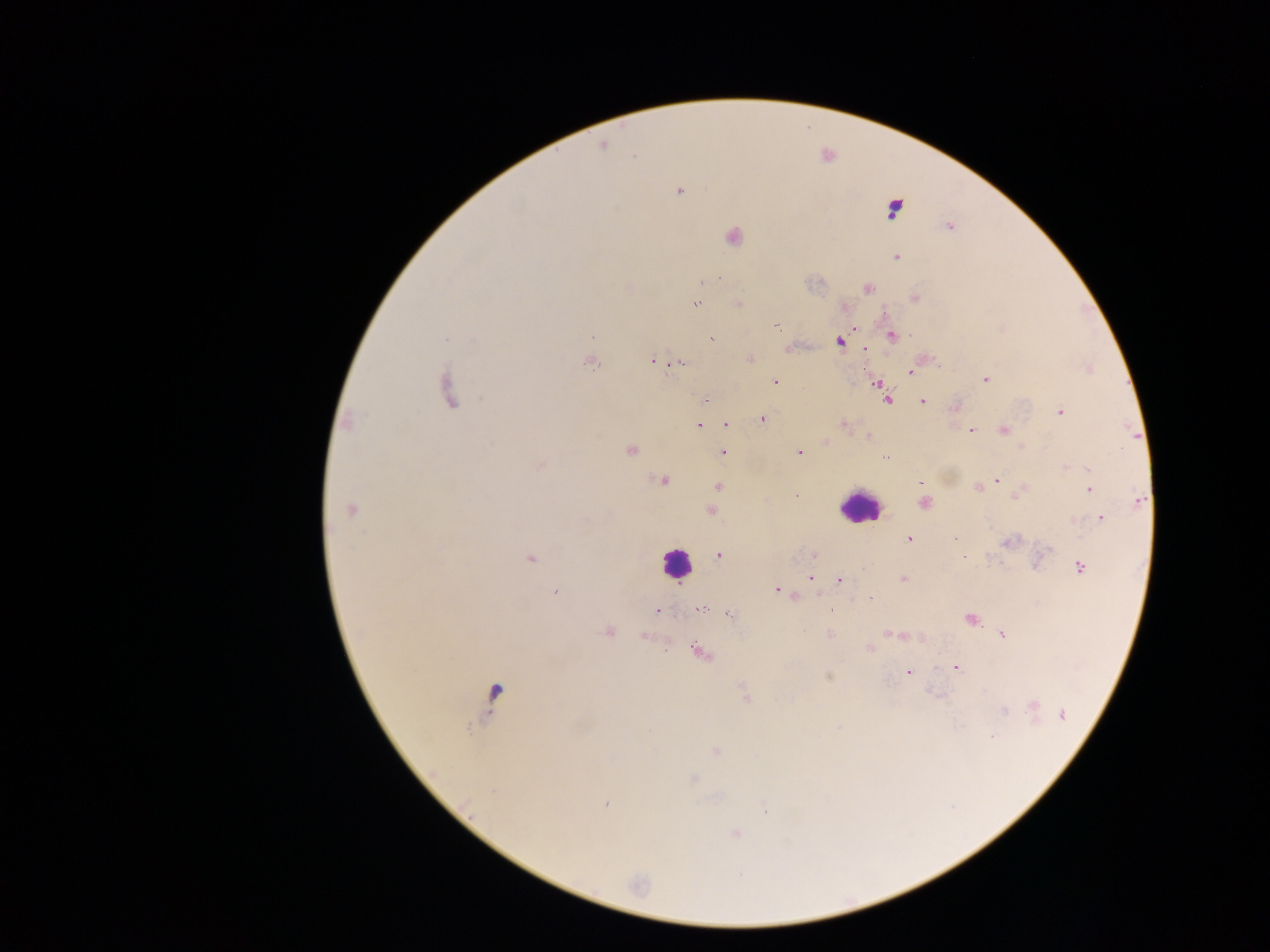
{
  "field_of_view": "single",
  "malaria_parasite_locations": "approximate centers as (x, y) in pixels: (603, 145), (678, 190), (948, 226), (731, 235), (895, 256), (704, 280), (868, 287), (914, 298), (694, 303), (738, 303), (845, 306), (777, 326), (853, 326), (891, 335), (712, 338), (838, 341), (788, 348), (865, 348), (749, 359), (588, 360), (653, 360), (678, 363), (1089, 368), (911, 372), (985, 379), (774, 382), (876, 383), (446, 390), (880, 391), (705, 399), (886, 400), (922, 400), (955, 407), (1059, 412), (762, 418), (347, 422), (726, 423), (698, 425), (843, 425), (1003, 430), (971, 431), (868, 436), (825, 442), (1021, 446), (630, 449), (723, 451), (798, 452), (884, 456), (539, 465), (1065, 467), (661, 479), (996, 479), (920, 482), (718, 486), (977, 486), (1089, 488), (1018, 493), (1139, 502), (923, 503), (350, 509), (710, 511), (1100, 518), (908, 539), (1009, 540), (1048, 549), (718, 555), (813, 555), (964, 557), (530, 558), (1080, 567), (810, 578), (903, 579), (840, 580), (777, 589), (556, 592), (793, 596), (870, 597), (698, 609), (831, 609), (657, 610), (727, 613), (970, 619), (608, 631), (829, 633), (888, 633), (899, 634), (1002, 634), (643, 637), (920, 637), (868, 647), (698, 651), (956, 668), (908, 672), (828, 676), (495, 693), (746, 698), (1033, 706), (1003, 710), (1061, 716), (991, 736), (715, 751), (692, 780), (606, 803), (734, 833)",
  "preparation": "thick blood smear",
  "image_size": "1270×952 pixels",
  "leukocyte_locations": "approximate centers as (x, y) in pixels: (893, 208), (859, 506), (676, 565)",
  "country": "Ghana",
  "capture": "mobile-phone photograph through a microscope"
}